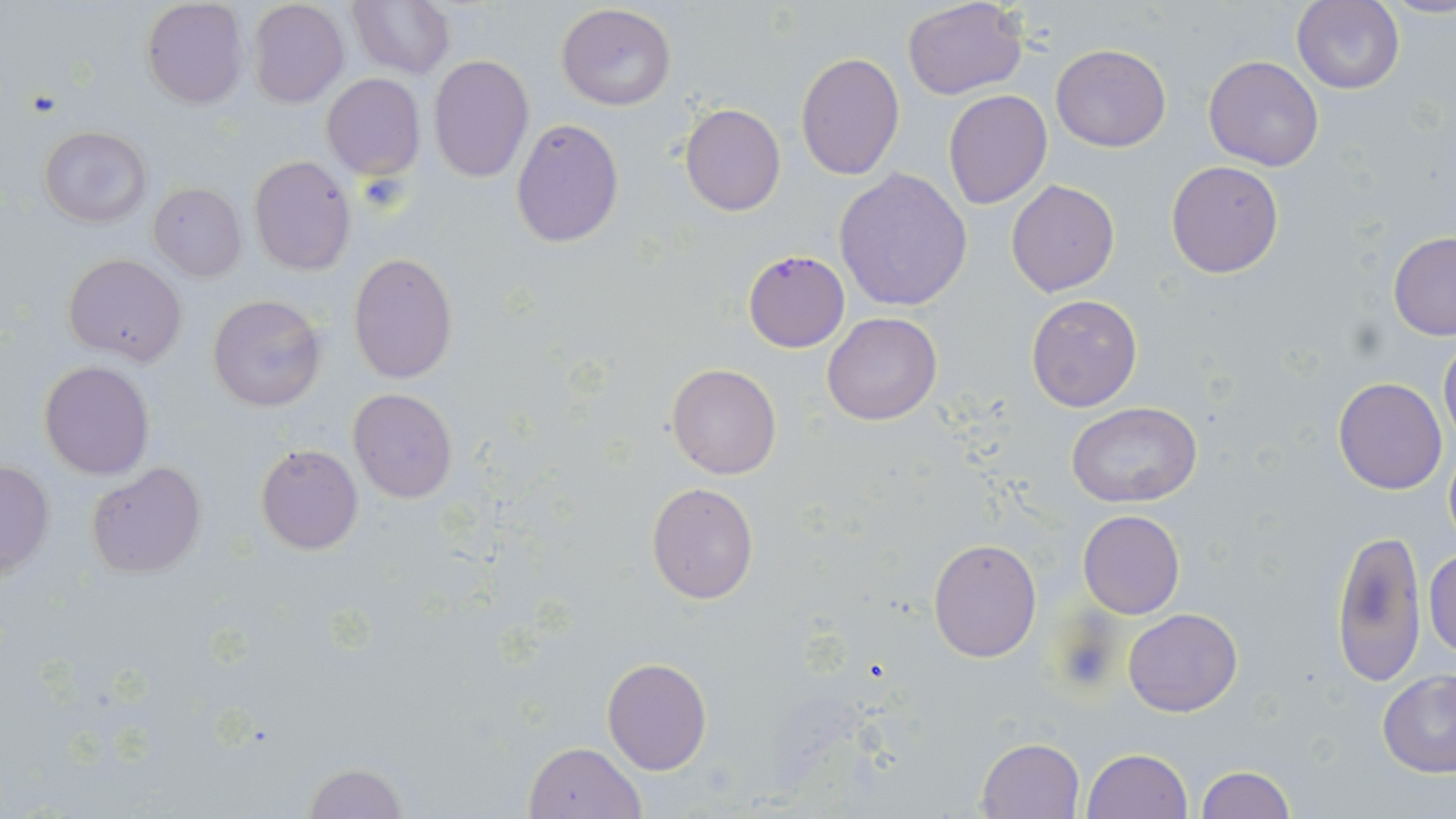

slide-level diagnosis = Plasmodium falciparum
magnification = 1000x
field of view = single
preparation = thin blood smear
modality = optical microscopy
uninfected red blood cell locations = approximate bounding boxes as (x1, y1, x2, y2) in pixels: (248, 0, 349, 108), (348, 0, 455, 80), (1291, 0, 1404, 94), (141, 1, 248, 109), (903, 1, 1026, 99), (555, 4, 677, 111), (1052, 43, 1170, 152), (795, 53, 905, 179), (428, 55, 534, 184), (1204, 55, 1323, 171), (321, 73, 425, 180), (943, 91, 1051, 209), (680, 102, 786, 216), (511, 118, 625, 249), (39, 126, 152, 228), (248, 154, 356, 277), (1165, 160, 1285, 277), (834, 168, 972, 312), (1005, 178, 1120, 297), (148, 182, 246, 282), (1387, 232, 1456, 340), (743, 250, 849, 353), (347, 251, 458, 384), (63, 253, 187, 367), (208, 294, 327, 412), (1026, 294, 1144, 412), (822, 311, 941, 424), (1439, 338, 1456, 445), (38, 360, 155, 479), (665, 363, 782, 480), (1333, 377, 1447, 495), (348, 388, 459, 505), (1067, 401, 1203, 509), (255, 444, 363, 554), (85, 460, 209, 579), (0, 462, 55, 579), (646, 483, 759, 602), (1078, 510, 1185, 619), (1330, 527, 1426, 687), (928, 537, 1042, 663), (1424, 549, 1456, 658), (1123, 608, 1243, 717), (602, 657, 712, 775), (1376, 670, 1456, 777), (976, 736, 1086, 819), (523, 741, 646, 819), (1081, 747, 1194, 818), (298, 761, 410, 818), (1194, 764, 1296, 819)
stain = May-Grünwald-Giemsa
image size = 1456×819 pixels